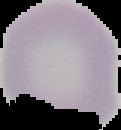
malaria_status: uninfected
preparation: thin blood film
image_size: 121×130 pixels
image_type: segmented cell region with the area outside set to black